Report the malaria status of this cell.
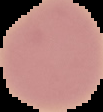

It is uninfected.

image size = 103×112 pixels
image type = cell region segmented out of the field of view; surrounding area masked to black
preparation = thin blood smear